State which parasite is depicted.
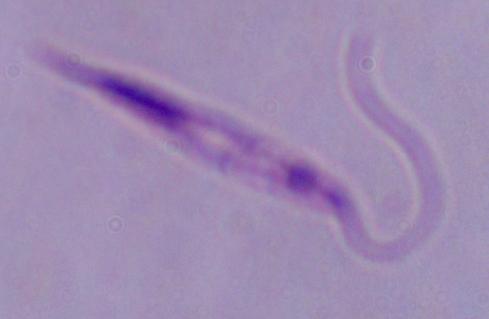
This is Leishmania.

Summary:
  - Modality: micrograph
  - Magnification: 1000x